Give the position of every malaria parasite.
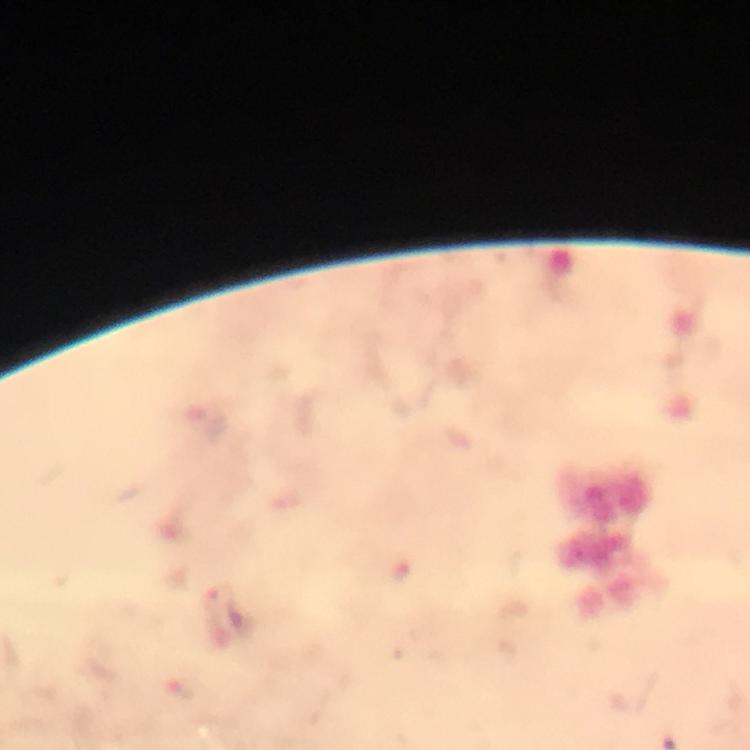
Approximate centers as [x, y] in pixels.
Malaria parasites: [218, 597].

Summary:
  - Magnification: 100x
  - Context: from a malaria diagnostic workup
  - Image size: 750×750 pixels
  - Cropped from: one field of view
  - Capture: smartphone photograph through a microscope
  - Stain: Giemsa
  - Immersion oil: applied
  - Preparation: thick blood film